Comment on the morphology of the red blood cells.
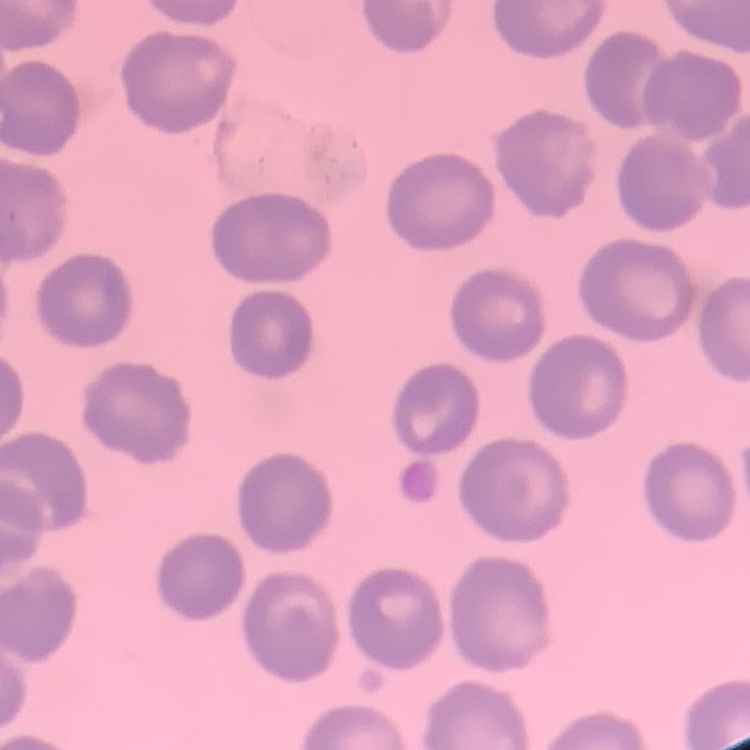
No rouleaux formation.

stain = Field's or Giemsa
image type = square crop of a larger photomicrograph
preparation = thin blood film